Name the parasite shown.
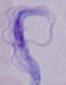

A trypanosome.

Summary:
  - Magnification: 1000x
  - Modality: photomicrograph